Evaluate for malaria.
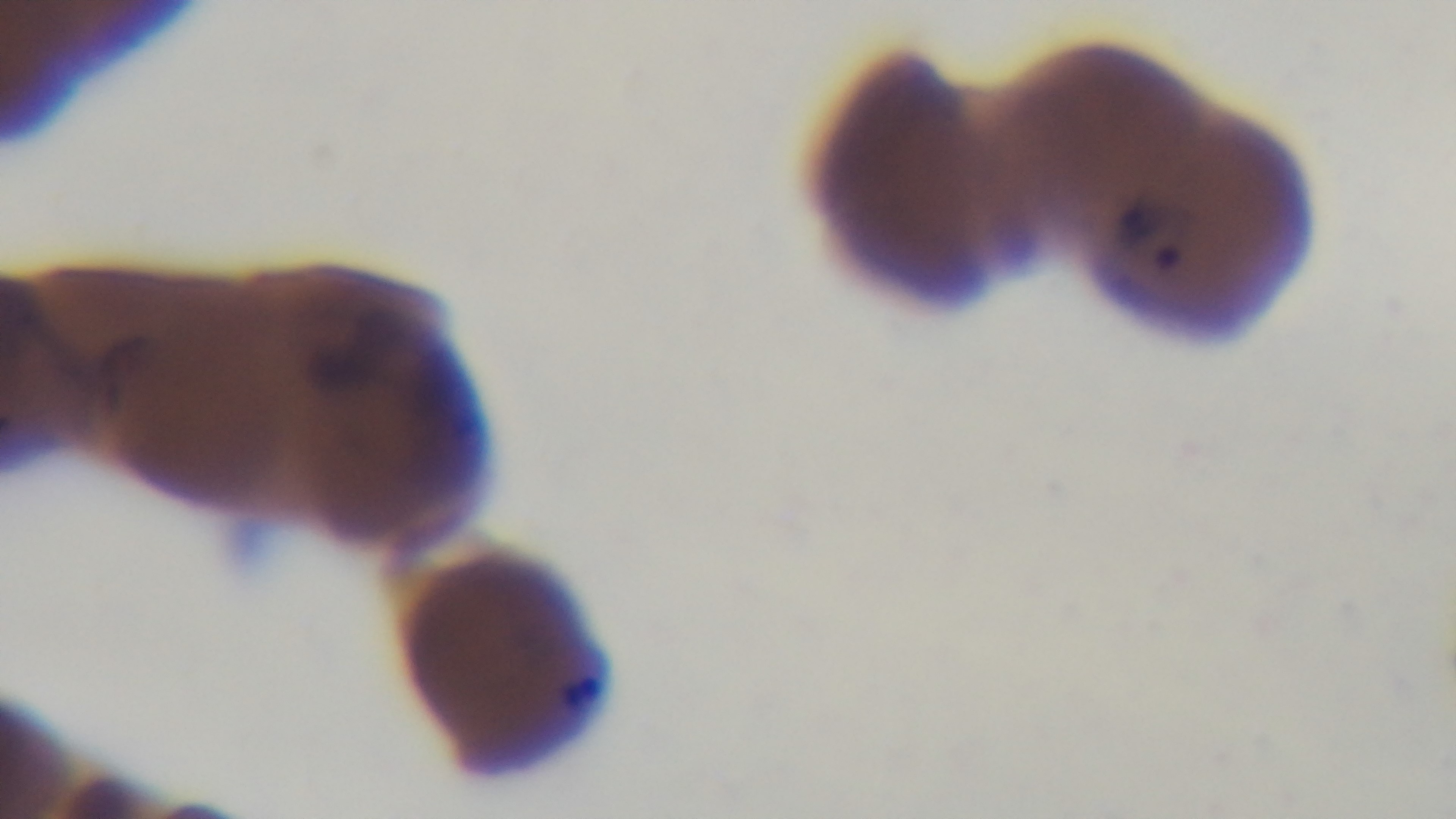

Positive.

preparation = thin
stain = Giemsa
objective = 100x oil immersion
capture = mounted 4K digital camera
field of view = single
modality = light microscopy